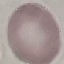
malaria status = uninfected
preparation = thin blood film
capture = smartphone camera at the microscope eyepiece
stain = Giemsa
image type = cell patch, automatically extracted from a larger field of view and resized to 64 × 64 pixels